Assess this cell for malaria.
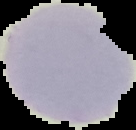

It is uninfected.

Summary:
  - Image size: 136×130 pixels
  - Preparation: thin blood smear
  - Image type: cell region segmented out of the field of view; surrounding area masked to black